State which parasite is depicted.
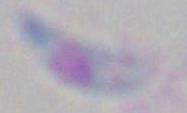

Toxoplasma gondii.

Summary:
  - Magnification: 1000x
  - Modality: micrograph